Give the extent of all Plasmodium falciparum-infected red blood cells.
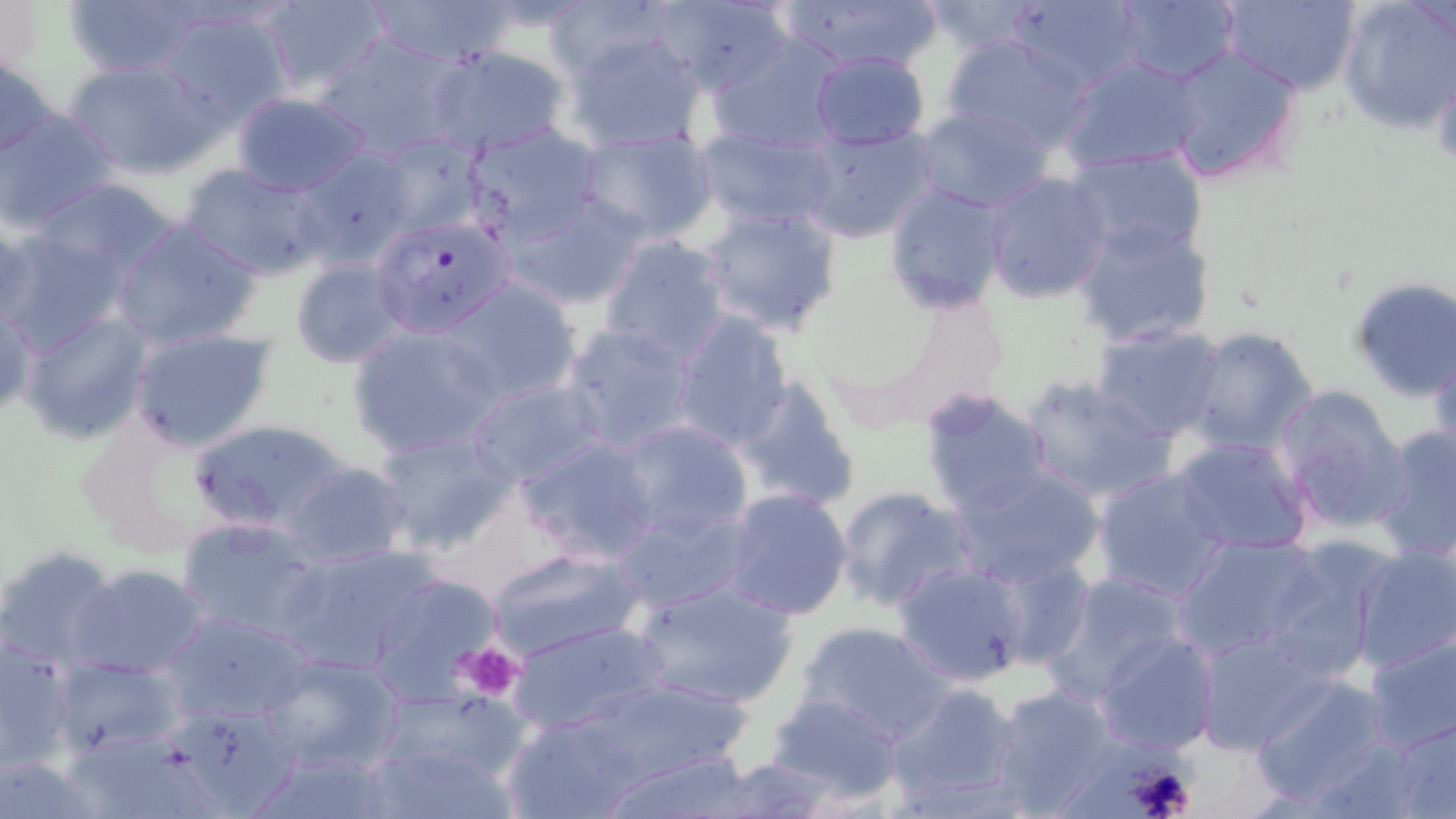
Approximate bounding boxes as (x1, y1, x2, y2) in pixels.
Plasmodium falciparum-infected red blood cells: (370, 213, 518, 339).

Platelet locations: (1430, 61, 1456, 170), (460, 641, 525, 701), (1125, 761, 1199, 819). Uninfected red blood cell locations: (0, 0, 43, 77), (60, 0, 214, 80), (252, 0, 390, 99), (365, 0, 519, 67), (538, 0, 676, 81), (654, 0, 793, 95), (775, 0, 944, 74), (1008, 0, 1146, 91), (1218, 0, 1362, 94), (1336, 0, 1456, 136), (1111, 1, 1240, 83), (149, 5, 293, 129), (562, 27, 708, 151), (942, 31, 1095, 153), (312, 32, 467, 161), (705, 35, 847, 156), (1161, 42, 1306, 186), (426, 45, 573, 157), (807, 51, 931, 149), (0, 54, 58, 161), (1061, 54, 1203, 174), (63, 56, 221, 177), (228, 91, 375, 197), (914, 105, 1053, 215), (0, 108, 121, 231), (460, 123, 603, 250), (798, 123, 937, 244), (572, 126, 719, 245), (695, 126, 844, 230), (368, 133, 488, 241), (1064, 146, 1209, 262), (292, 147, 412, 267), (178, 161, 331, 282), (982, 171, 1112, 304), (28, 177, 181, 288), (882, 181, 1011, 315), (506, 192, 649, 310), (697, 203, 845, 336), (1072, 216, 1217, 349), (109, 217, 260, 351), (0, 228, 134, 355), (597, 234, 732, 364), (290, 256, 410, 369), (1347, 276, 1456, 401), (441, 277, 583, 405), (890, 288, 1011, 415), (1, 294, 36, 420), (18, 309, 154, 444), (668, 312, 794, 449), (346, 322, 508, 458), (559, 322, 699, 454), (1092, 323, 1227, 443), (1184, 325, 1319, 456), (127, 326, 276, 451), (1430, 337, 1456, 466), (1018, 375, 1177, 506), (730, 378, 862, 512), (463, 379, 606, 488), (1272, 383, 1410, 530), (917, 388, 1055, 517), (190, 416, 353, 540), (614, 417, 753, 542), (1371, 424, 1456, 561), (373, 429, 520, 556), (516, 435, 661, 563), (1169, 435, 1316, 556), (280, 462, 414, 569), (950, 465, 1104, 587), (1091, 467, 1232, 604), (833, 485, 978, 612), (722, 487, 854, 620), (613, 504, 752, 613), (177, 517, 326, 643), (1171, 534, 1324, 661), (1260, 538, 1398, 679), (1349, 542, 1456, 673), (275, 543, 444, 675), (0, 546, 118, 671), (483, 546, 645, 663), (991, 556, 1094, 669), (892, 561, 1032, 686), (68, 564, 211, 681), (357, 565, 507, 705), (1041, 571, 1192, 704), (628, 575, 798, 709), (159, 609, 313, 727), (507, 617, 672, 739), (796, 621, 954, 745), (1191, 628, 1332, 752), (1362, 628, 1455, 755), (1093, 630, 1218, 755), (0, 637, 77, 775), (258, 649, 407, 775), (53, 656, 185, 760), (1248, 673, 1398, 808), (883, 682, 1028, 813), (543, 683, 757, 818), (986, 683, 1120, 817), (371, 687, 533, 799), (765, 690, 905, 806), (168, 703, 301, 815), (1386, 714, 1456, 818), (362, 737, 518, 818), (595, 746, 761, 818), (1, 750, 108, 819), (706, 757, 843, 817). Slide-level diagnosis: Plasmodium falciparum. Image is 1456×819 pixels. One field of a larger specimen. May-Grünwald-Giemsa-stained preparation. 1000x magnification. Thin blood smear. Optical microscopy.